Identify the cell.
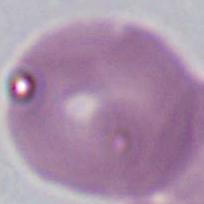
This is an erythrocyte.

Summary:
  - Magnification: 1000x
  - Modality: photomicrograph